Assess this cell for malaria.
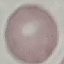
Uninfected.

Thin blood film. Giemsa-stained preparation. Automatically extracted cell patch, resized to 64 × 64 pixels. Acquired by smartphone through the microscope eyepiece.